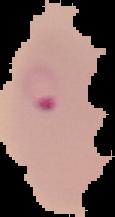

{
  "malaria_status": "parasitized",
  "preparation": "thin blood smear",
  "image_type": "segmented cell region with the area outside set to black",
  "image_size": "115×217 pixels"
}